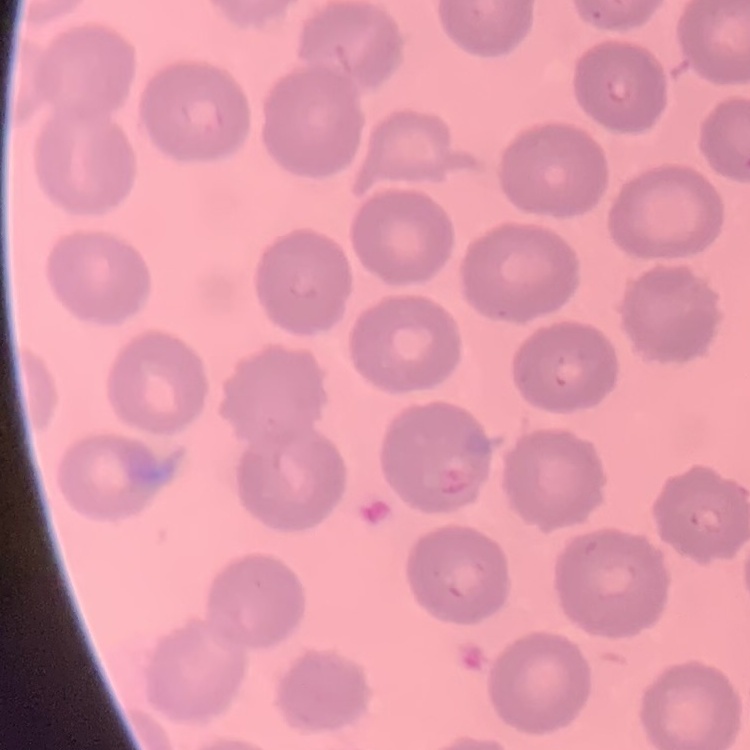 The erythrocytes exhibit no rouleaux formation. Square crop of a larger photomicrograph. Field's or Giemsa stain. Thin blood smear.